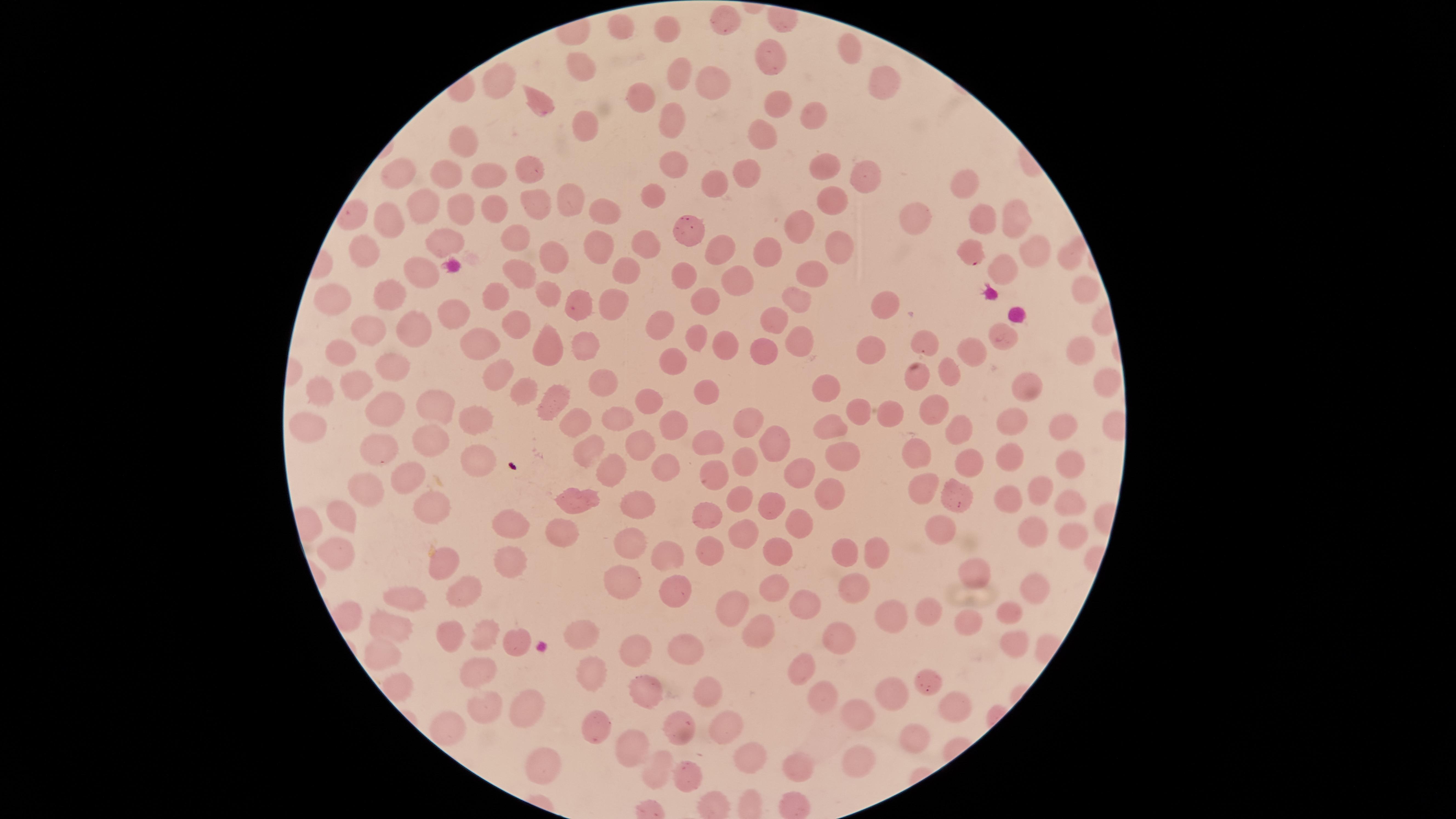

Approximate marker points as (x, y) in pixels. Uninfected RBCs: (726, 26), (617, 27), (669, 28), (848, 51), (770, 59), (579, 69), (676, 71), (498, 81), (708, 81), (878, 84), (643, 97), (537, 103), (776, 105), (810, 116), (669, 117), (577, 127), (759, 135), (463, 140), (673, 165), (822, 165), (526, 169), (451, 170), (744, 170), (859, 175), (400, 176), (487, 176), (965, 182), (715, 183), (652, 194), (835, 195), (565, 198), (533, 205), (424, 206), (603, 208), (485, 209), (455, 210), (1014, 216), (385, 218), (916, 219), (984, 219), (805, 223), (691, 233), (512, 239), (644, 242), (436, 243), (835, 243), (602, 247), (362, 248), (764, 250), (1038, 252), (715, 253), (1070, 254), (551, 258), (1009, 265), (625, 266), (815, 272), (517, 273), (416, 274), (685, 275), (734, 282), (1082, 291), (388, 294), (546, 294), (330, 296), (492, 296), (799, 296), (708, 298), (578, 300), (613, 302), (884, 307), (450, 313), (775, 320), (515, 324), (664, 324), (368, 328), (408, 331), (1008, 332), (693, 334), (796, 340), (726, 341), (482, 342), (586, 343), (925, 343), (547, 344), (978, 348), (340, 350), (868, 350), (1078, 350), (764, 351), (673, 356), (392, 365), (951, 372), (494, 374), (920, 377), (598, 379), (358, 381), (1026, 382), (321, 385), (1104, 385), (705, 387), (833, 388), (516, 389), (646, 402), (439, 404), (548, 404), (932, 407), (384, 409), (861, 410), (888, 413), (613, 416), (305, 418), (474, 418), (745, 419), (1014, 420), (574, 421), (962, 422), (672, 425), (832, 425), (1066, 429), (433, 441), (772, 441), (643, 443), (703, 444), (376, 449), (918, 452), (841, 455), (971, 455), (477, 457), (1008, 459), (746, 461), (664, 465), (1068, 468), (612, 471), (802, 472), (401, 477), (715, 480), (369, 489), (952, 489), (918, 491), (1033, 492), (828, 493), (580, 497), (432, 501), (1001, 502), (738, 503), (636, 505), (1069, 505), (769, 506), (705, 516), (339, 517), (512, 525), (797, 525), (938, 526), (1031, 531), (744, 532), (558, 535), (1065, 538), (630, 545), (774, 551), (851, 551), (876, 552), (331, 553), (705, 555), (668, 559), (512, 563), (444, 564), (977, 572), (622, 584), (1031, 588), (771, 589), (852, 589), (465, 592), (672, 593), (405, 598), (805, 599), (731, 611), (930, 613), (1010, 614), (890, 618), (966, 622), (387, 627), (760, 628), (582, 631), (447, 633), (480, 638), (836, 639), (1014, 643), (510, 645), (674, 648), (633, 650), (376, 655), (805, 668), (584, 670), (477, 672), (928, 676), (644, 687), (704, 693), (894, 693), (820, 701), (524, 702), (948, 702), (485, 710), (860, 716), (720, 722), (444, 723), (593, 726), (675, 726), (912, 738), (634, 747), (751, 754), (854, 763), (540, 768), (655, 769), (798, 769), (690, 774). Parasitized RBCs: (970, 254). One field of view of the specimen. Image is 1456×819 pixels. Smartphone photograph through the microscope eyepiece. Thin blood smear. Giemsa-stained preparation. Presence: malaria parasites seen. Circular visible region. Species: Plasmodium falciparum.